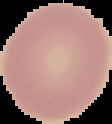
Summary:
  - Image type: segmented cell region with the area outside set to black
  - Malaria status: uninfected
  - Image size: 112×124 pixels
  - Preparation: thin blood film